Report the malaria status of this cell.
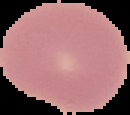
It is uninfected.

Image is 130×115 pixels. From a thin blood film. The area outside the segmented cell region is set to black.